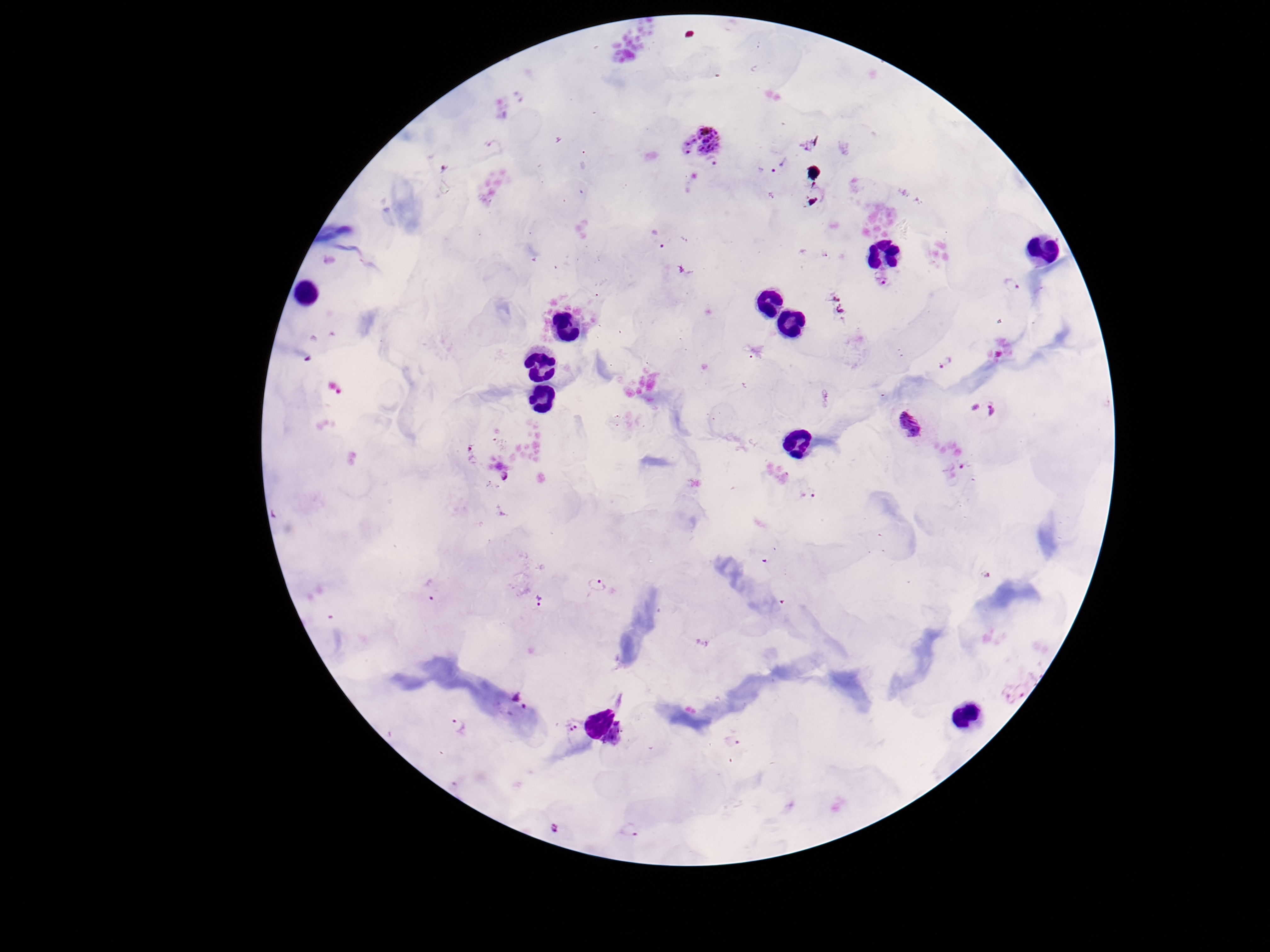
Approximate object centers, in pixels from the top-left corner. Plasmodium parasite locations: (x=700, y=135), (x=715, y=164), (x=778, y=166), (x=1011, y=283), (x=946, y=363), (x=982, y=407), (x=908, y=422), (x=471, y=454), (x=963, y=463), (x=505, y=475), (x=809, y=492), (x=598, y=584), (x=433, y=588), (x=537, y=601), (x=516, y=696), (x=457, y=724), (x=573, y=725), (x=732, y=741), (x=555, y=827), (x=632, y=830). Image is 1270×952 pixels. Patient malaria status: infected. 100x magnification. Photographed through the microscope eyepiece with a smartphone camera. Thick blood smear. Giemsa-stained preparation. One field from this slide.